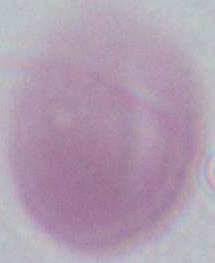

An erythrocyte is shown. 1000x magnification. Micrograph.